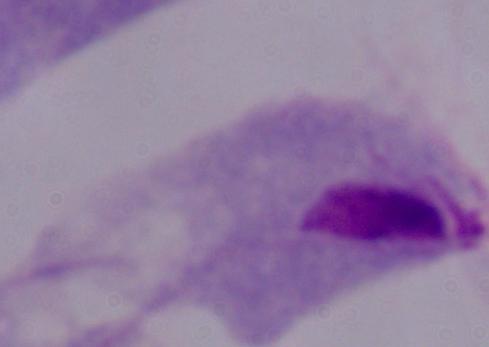

modality = photomicrograph
magnification = 1000x
identification = trichomonad